Outline each uninfected red blood cell.
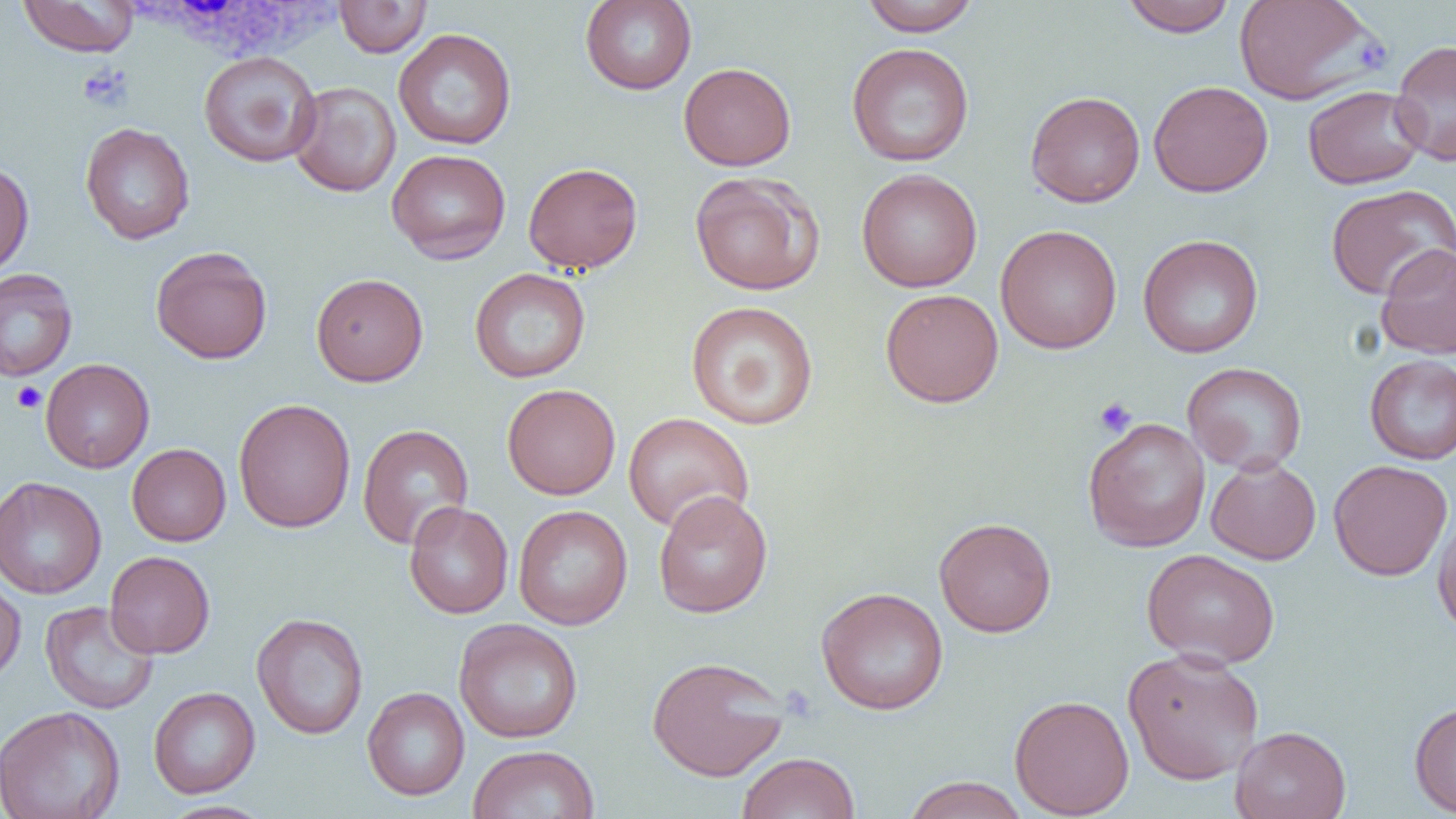
Approximate bounding boxes as [x1, y1, x2, y2] in pixels.
Uninfected red blood cells: [17, 0, 140, 57], [334, 0, 432, 57], [580, 0, 697, 95], [860, 0, 981, 36], [1120, 0, 1238, 37], [1234, 0, 1380, 105], [393, 28, 517, 150], [1390, 39, 1456, 166], [846, 42, 974, 166], [198, 50, 322, 167], [679, 62, 796, 171], [1148, 80, 1273, 197], [288, 81, 401, 197], [1302, 84, 1427, 189], [1025, 90, 1146, 207], [80, 122, 195, 244], [386, 148, 511, 263], [0, 160, 34, 278], [523, 161, 643, 274], [856, 168, 983, 292], [689, 171, 825, 296], [1325, 184, 1456, 301], [995, 224, 1122, 354], [1137, 234, 1264, 358], [1375, 242, 1456, 359], [150, 246, 272, 364], [469, 268, 591, 382], [0, 269, 78, 381], [311, 273, 429, 386], [879, 288, 1004, 407], [685, 300, 819, 430], [1364, 355, 1456, 464], [41, 358, 154, 473], [1182, 362, 1307, 474], [502, 384, 621, 499], [233, 398, 356, 533], [623, 412, 754, 533], [1082, 418, 1211, 552], [357, 423, 474, 549], [127, 443, 231, 546], [1206, 456, 1321, 565], [1328, 459, 1453, 581], [1, 476, 107, 599], [653, 490, 773, 618], [403, 500, 513, 619], [1432, 503, 1456, 640], [513, 505, 633, 629], [933, 516, 1057, 637], [1141, 548, 1280, 668], [105, 551, 215, 658], [0, 572, 26, 686], [815, 586, 949, 714], [40, 600, 159, 714], [251, 612, 368, 739], [453, 618, 583, 743], [1122, 648, 1265, 785], [647, 655, 791, 781], [362, 686, 469, 801], [148, 687, 260, 798], [1009, 694, 1135, 818], [1409, 700, 1456, 817], [0, 705, 126, 819], [1230, 725, 1351, 819], [468, 744, 600, 819], [737, 752, 861, 819], [902, 776, 1029, 819], [159, 800, 273, 819].

Summary:
  - White blood cell locations: [123, 0, 345, 64]
  - Platelet locations: [1354, 36, 1392, 73], [77, 64, 133, 111], [11, 381, 47, 413], [1094, 397, 1137, 438]
  - Slide-level diagnosis: no evidence of blood parasites
  - Preparation: thin blood smear
  - Field of view: one of a larger specimen
  - Magnification: 1000x
  - Image size: 1456×819 pixels
  - Modality: light microscopy